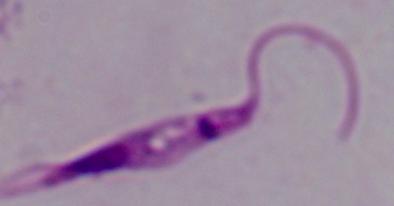
modality = photomicrograph
magnification = 1000x
identification = Leishmania